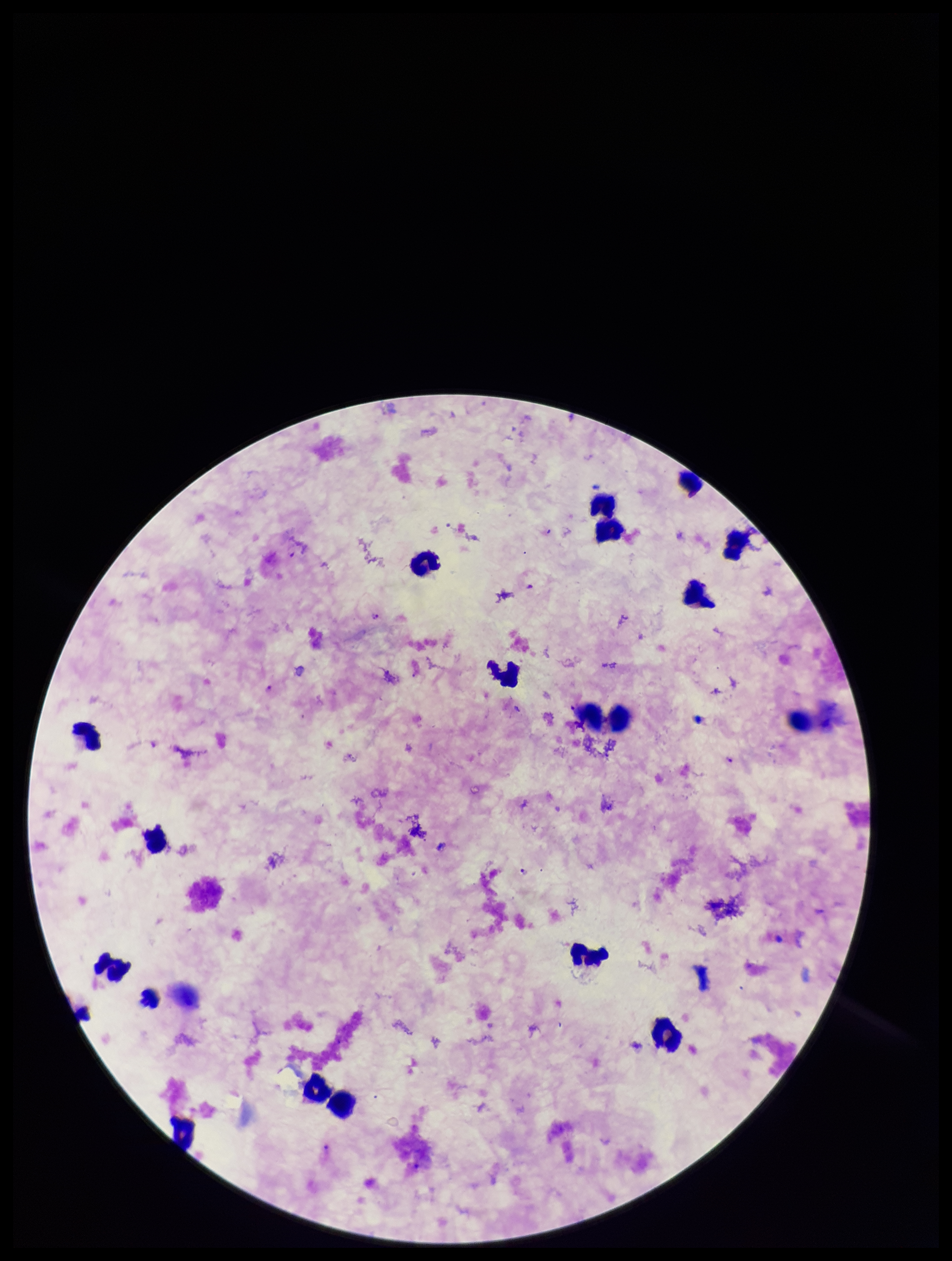
Summary:
  - Capture: smartphone photograph through the microscope eyepiece
  - Preparation: thick blood smear
  - Stain: Giemsa
  - Parasite count: 5
  - Image size: 952×1261 pixels
  - Species reported for this patient: Plasmodium falciparum
  - Field of view: one from this slide
  - Plasmodium parasites: detected
  - Leukocyte count: 19
  - Patient malaria status: positive